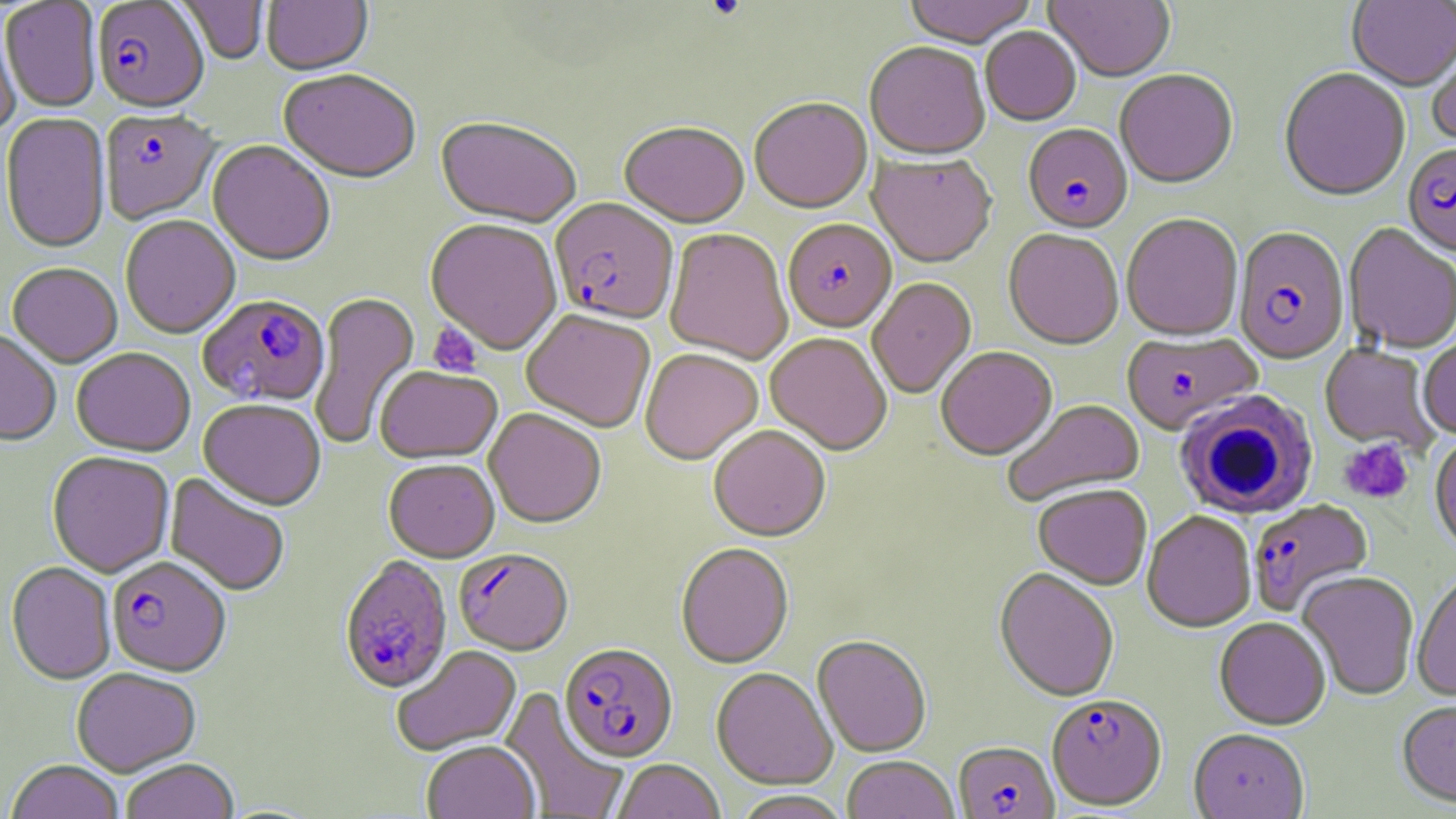
Summary:
  - Coordinate format: approximate bounding boxes as (x1, y1, x2, y2) in pixels
  - Platelet locations: (427, 323, 482, 378), (1339, 439, 1413, 504)
  - Uninfected red blood cell locations: (175, 0, 268, 66), (262, 0, 373, 78), (902, 0, 1037, 51), (1045, 0, 1175, 85), (1347, 0, 1456, 93), (1, 2, 101, 113), (0, 16, 21, 138), (980, 28, 1081, 128), (1427, 36, 1456, 149), (864, 45, 991, 163), (1279, 70, 1410, 203), (279, 72, 420, 187), (1115, 72, 1238, 191), (750, 100, 873, 215), (0, 114, 111, 255), (435, 119, 581, 230), (619, 125, 749, 231), (207, 142, 335, 268), (867, 155, 996, 270), (1121, 215, 1243, 343), (120, 217, 240, 341), (425, 221, 562, 356), (1344, 224, 1456, 355), (665, 230, 792, 366), (1003, 230, 1124, 352), (7, 264, 122, 370), (867, 279, 977, 400), (310, 292, 419, 451), (521, 312, 655, 434), (0, 332, 61, 448), (765, 334, 891, 456), (1417, 338, 1456, 440), (1320, 344, 1439, 453), (936, 348, 1058, 461), (71, 349, 195, 459), (640, 350, 763, 467), (375, 367, 501, 466), (198, 400, 326, 513), (1003, 401, 1146, 507), (484, 410, 605, 530), (708, 427, 830, 544), (1430, 437, 1456, 555), (47, 453, 174, 579), (384, 461, 500, 563), (164, 474, 289, 597), (1033, 486, 1152, 591), (1142, 512, 1256, 633), (676, 544, 794, 670), (5, 562, 116, 686), (994, 569, 1119, 704), (1297, 572, 1420, 701), (1412, 573, 1455, 703), (1214, 619, 1330, 731), (812, 637, 932, 758), (392, 646, 521, 757), (72, 668, 202, 778), (711, 669, 837, 791), (499, 687, 629, 819), (1397, 701, 1456, 811), (1189, 731, 1309, 819), (422, 742, 539, 819), (842, 757, 959, 819), (121, 760, 239, 819), (612, 760, 724, 819), (5, 762, 124, 819), (731, 791, 853, 819)
  - Plasmodium falciparum-infected red blood cell locations: (92, 1, 209, 116), (100, 111, 221, 226), (1023, 125, 1133, 236), (1402, 144, 1456, 261), (549, 199, 679, 328), (786, 221, 900, 334), (1233, 228, 1349, 366), (197, 296, 330, 409), (1122, 333, 1262, 436), (1248, 501, 1373, 617), (454, 551, 574, 656), (107, 558, 231, 678), (339, 558, 452, 696), (559, 645, 678, 764), (1047, 695, 1167, 812), (953, 742, 1059, 818)
  - White blood cell locations: (1174, 392, 1319, 520)
  - Slide-level diagnosis: Plasmodium falciparum
  - Magnification: 1000x
  - Modality: light microscopy
  - Field of view: one of a larger specimen
  - Stain: May-Grünwald-Giemsa
  - Preparation: thin blood smear
  - Image size: 1456×819 pixels